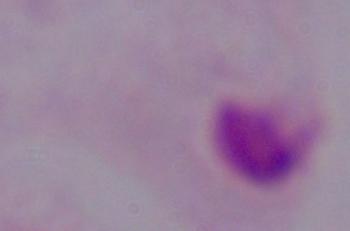

Micrograph. Captured at 1000x magnification. A trichomonad is shown.